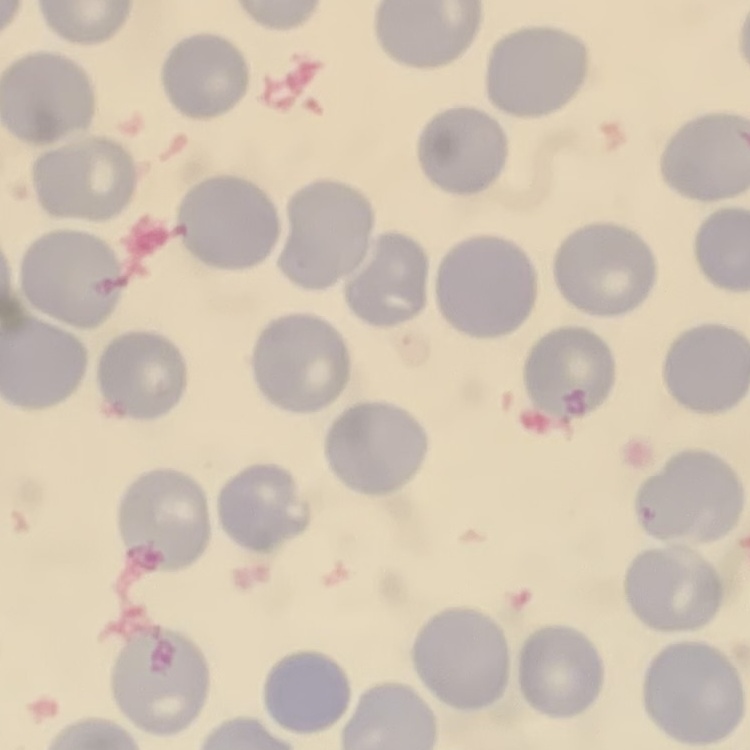
The red blood cells show no rouleaux formation. Thin blood film. Square crop of a larger photomicrograph. Field's or Giemsa stain.